State which parasite is depicted.
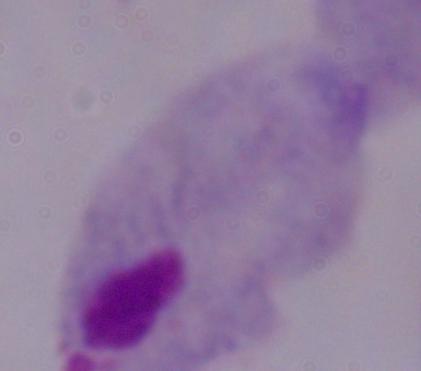
A trichomonad.

modality = photomicrograph
magnification = 1000x